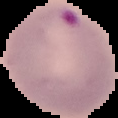

image size = 118×118 pixels
preparation = thin blood smear
image type = segmented cell region with the area outside set to black
result = malaria parasites detected